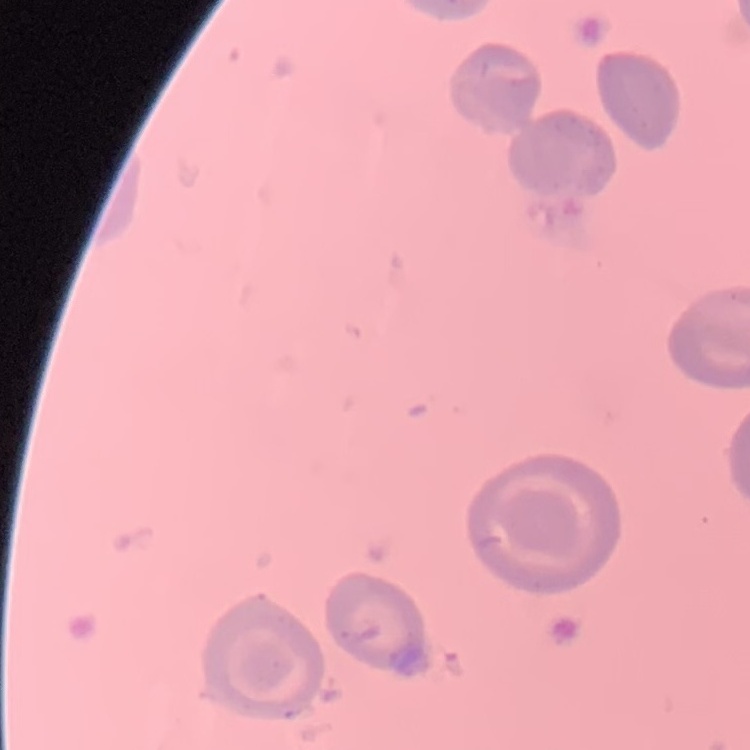 The erythrocytes show no rouleaux formation. Square crop of a larger photomicrograph. Stained with either Field's or Giemsa. Thin blood smear.